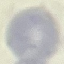

{
  "malaria_status": "uninfected",
  "image_type": "cell patch, automatically extracted from a larger field of view and resized to 64 × 64 pixels",
  "stain": "Giemsa",
  "preparation": "thin blood smear",
  "capture": "smartphone through the microscope eyepiece"
}